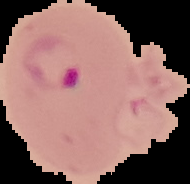

image type = segmented cell region with the area outside set to black
image size = 190×184 pixels
result = malaria parasites detected
preparation = thin blood film